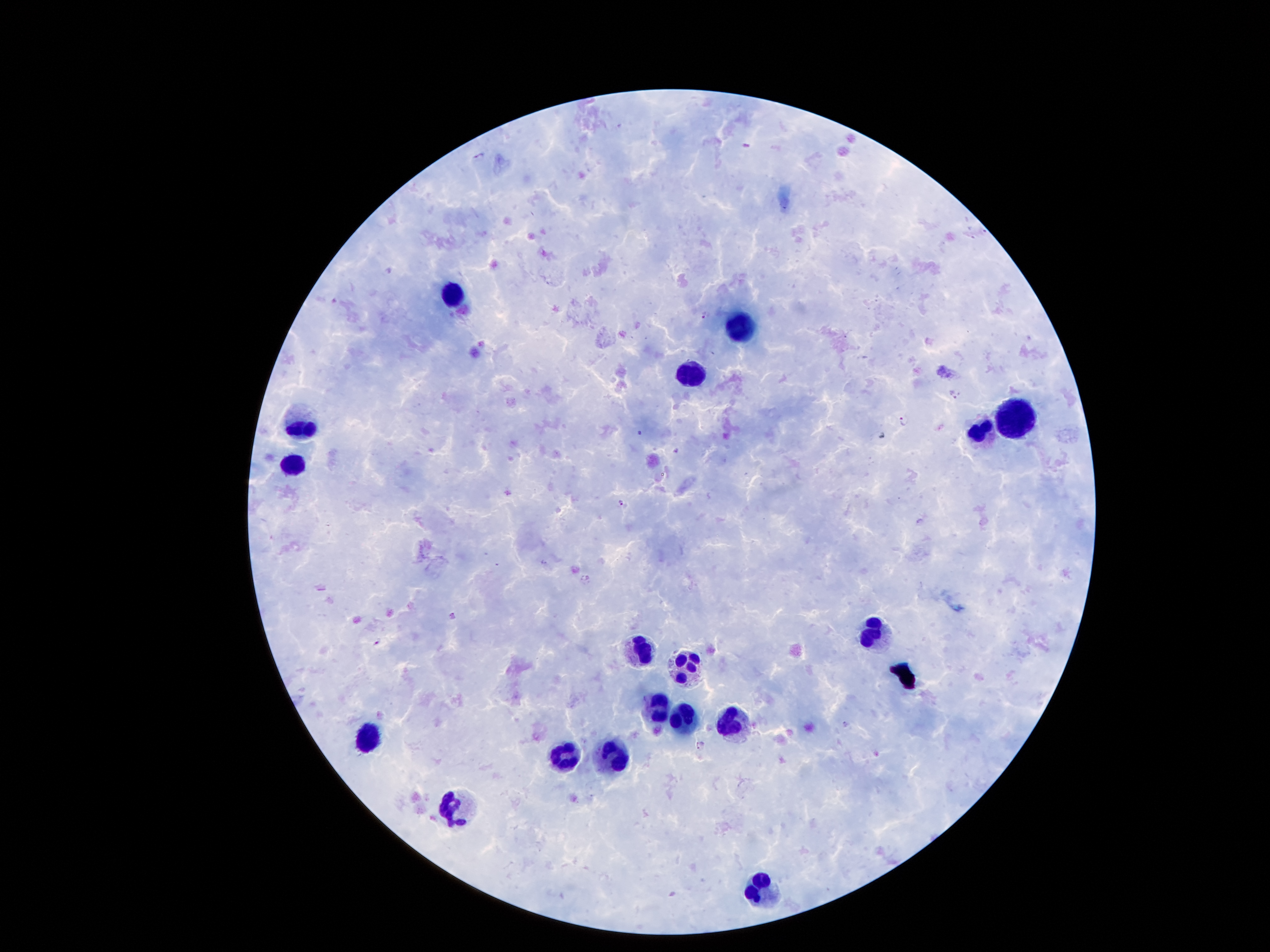 Approximate centers as [x, y] in pixels. Leukocyte locations: [451, 294], [742, 324], [693, 370], [1019, 420], [302, 422], [979, 434], [295, 464], [876, 629], [646, 652], [688, 659], [653, 708], [685, 715], [727, 724], [367, 738], [614, 755], [562, 757], [455, 805], [759, 884]. Malaria parasite locations: [747, 144], [478, 156], [706, 315], [954, 394], [904, 422], [639, 432], [676, 450], [620, 501], [378, 643], [700, 745]. Single field of view. Image is 1270×952 pixels. Giemsa-stained preparation. Patient malaria status: positive for Plasmodium falciparum. 100x magnification. Photographed through the microscope eyepiece with a smartphone camera. Thick blood smear.